Outline each Plasmodium falciparum-infected red blood cell.
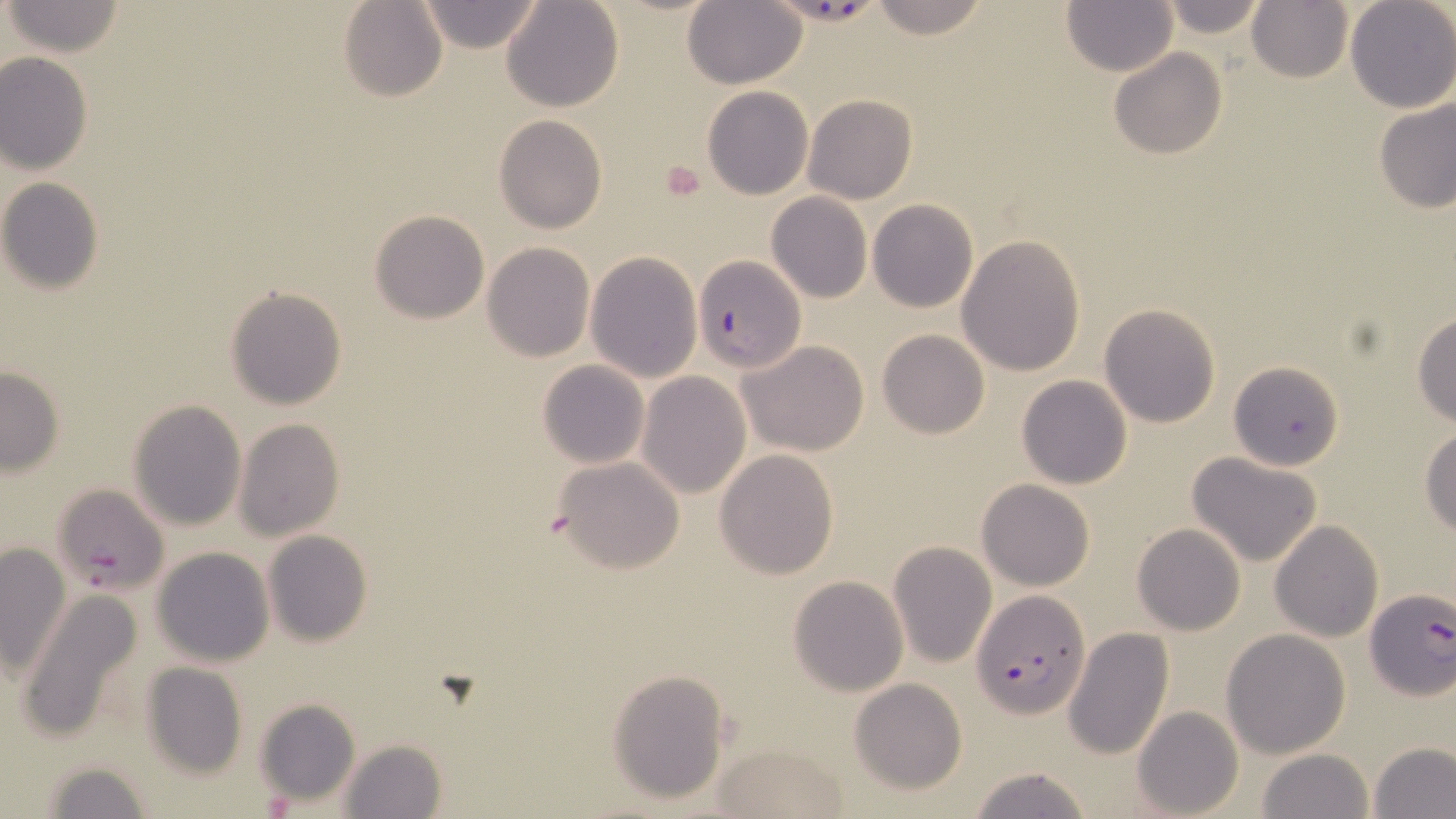
Approximate bounding boxes as [x1, y1, x2, y2] in pixels.
Plasmodium falciparum-infected red blood cells: [796, 0, 874, 29], [693, 256, 804, 373], [52, 483, 170, 598], [1362, 589, 1455, 704], [972, 590, 1090, 718].

slide-level diagnosis = Plasmodium falciparum
preparation = thin blood film
image size = 1456×819 pixels
stain = May-Grünwald-Giemsa
magnification = 1000x
uninfected red blood cell locations = approximate bounding boxes as [x1, y1, x2, y2] in pixels: [337, 0, 447, 102], [417, 0, 545, 53], [501, 0, 623, 112], [865, 0, 991, 42], [1155, 0, 1269, 38], [1246, 0, 1354, 84], [2, 1, 126, 56], [1061, 1, 1178, 77], [1345, 1, 1455, 114], [682, 2, 807, 88], [1109, 48, 1227, 160], [0, 52, 93, 174], [701, 86, 812, 199], [803, 94, 917, 204], [1375, 98, 1456, 215], [494, 114, 606, 234], [0, 178, 105, 295], [766, 192, 872, 302], [868, 199, 979, 313], [371, 210, 490, 324], [956, 235, 1087, 377], [482, 242, 596, 363], [586, 251, 703, 382], [225, 286, 346, 409], [1097, 304, 1221, 428], [1410, 313, 1456, 427], [876, 329, 990, 440], [739, 340, 869, 457], [537, 361, 649, 469], [1229, 361, 1343, 472], [0, 366, 64, 475], [637, 371, 751, 500], [1016, 375, 1133, 489], [129, 398, 246, 531], [233, 418, 345, 540], [1421, 427, 1456, 535], [713, 449, 839, 579], [1188, 452, 1323, 567], [552, 456, 684, 573], [978, 479, 1094, 590], [1269, 520, 1383, 642], [1131, 523, 1245, 635], [263, 530, 372, 647], [888, 541, 997, 666], [0, 543, 72, 678], [152, 547, 275, 665], [789, 576, 907, 695], [16, 590, 146, 743], [1064, 628, 1174, 759], [1220, 629, 1350, 758], [142, 663, 246, 780], [607, 670, 731, 804], [849, 678, 969, 795], [255, 698, 361, 807], [1133, 706, 1243, 819], [336, 739, 448, 818], [1370, 741, 1456, 818], [715, 743, 850, 818], [1256, 749, 1376, 819], [37, 758, 152, 818], [967, 764, 1093, 819]
modality = optical microscopy
platelet locations = approximate bounding boxes as [x1, y1, x2, y2] in pixels: [658, 160, 708, 203]
field of view = one of a larger specimen